Identify the parasite.
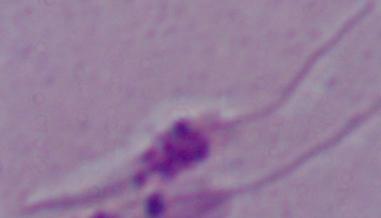
This is Leishmania.

magnification = 1000x
modality = micrograph